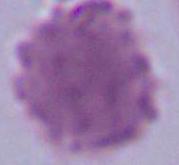

Summary:
  - Identification: erythrocyte
  - Modality: micrograph
  - Magnification: 1000x